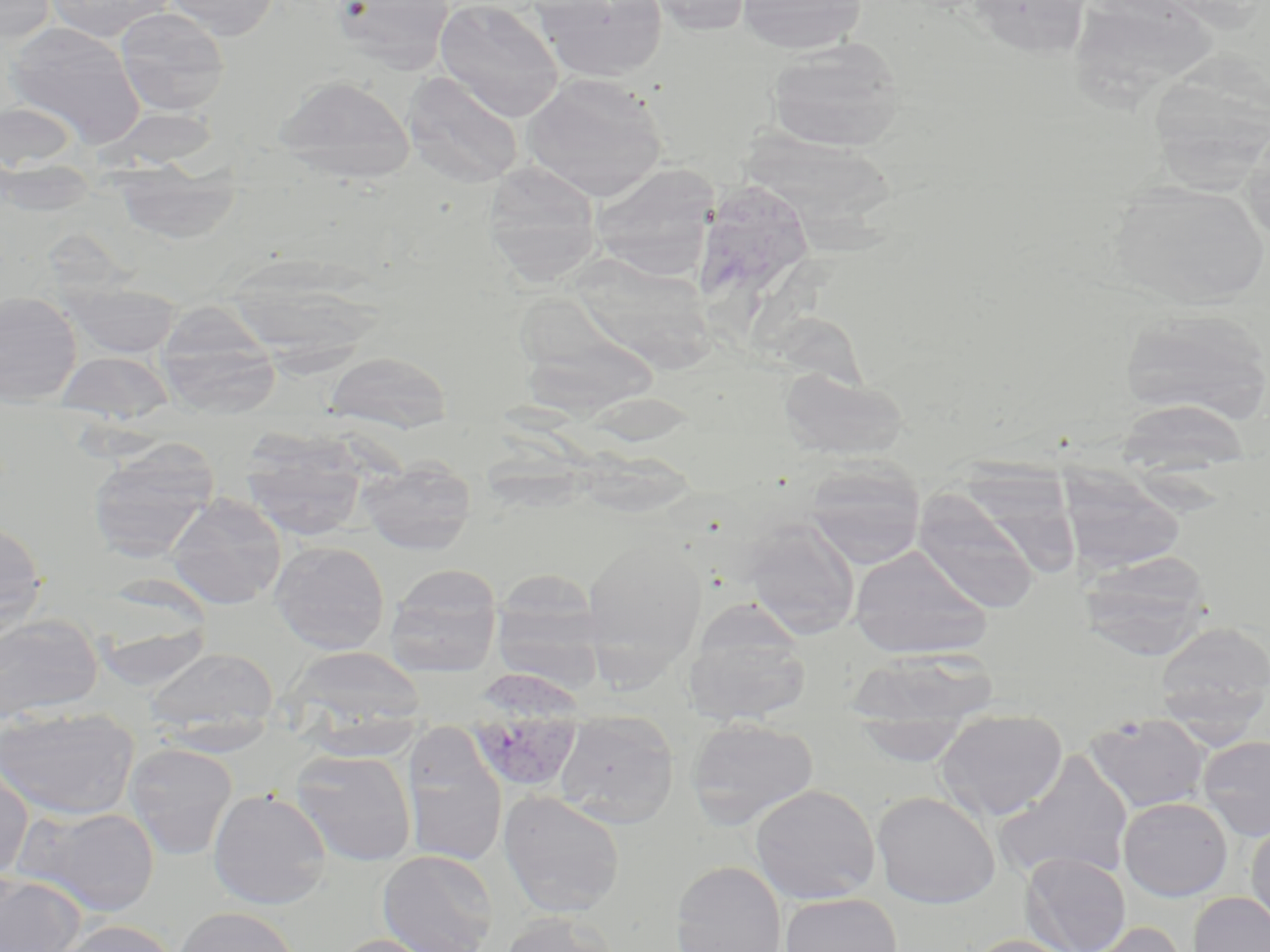

Summary:
  - Coordinate format: approximate bounding boxes as (x1,y1)-(x2,y2) corner pairs in pixels
  - Uninfected red blood cell locations: (0,0)-(56,44), (44,0)-(173,41), (162,0)-(280,40), (332,0)-(454,73), (434,0)-(564,121), (535,0)-(669,83), (643,0)-(754,36), (736,0)-(868,54), (966,0)-(1096,59), (1073,3)-(1223,117), (115,6)-(229,116), (5,21)-(146,147), (766,38)-(905,152), (1151,54)-(1270,206), (402,72)-(524,188), (521,73)-(668,201), (273,74)-(415,182), (0,101)-(79,173), (98,107)-(222,172), (1241,120)-(1270,244), (740,132)-(895,231), (112,158)-(240,245), (483,161)-(602,286), (590,163)-(722,279), (699,166)-(802,335), (1107,181)-(1268,309), (570,252)-(726,384), (229,256)-(389,379), (62,281)-(182,359), (0,291)-(83,406), (503,295)-(653,425), (155,304)-(281,417), (1119,308)-(1269,426), (56,351)-(175,425), (324,351)-(451,432), (779,367)-(908,461), (1115,399)-(1252,482), (239,428)-(372,541), (88,439)-(218,561), (358,456)-(477,555), (805,459)-(925,569), (960,466)-(1082,579), (1059,468)-(1186,576), (912,489)-(1040,614), (165,494)-(287,610), (0,520)-(48,639), (744,521)-(860,640), (582,535)-(707,678), (270,541)-(390,654), (849,545)-(990,659), (1079,550)-(1212,658), (385,565)-(502,675), (491,570)-(605,687), (0,613)-(103,723), (88,614)-(215,690), (684,615)-(810,726), (1155,621)-(1270,728), (282,646)-(425,739), (144,647)-(279,737), (848,649)-(997,731), (0,706)-(139,820), (935,708)-(1069,821), (555,712)-(679,827), (1085,712)-(1211,813), (854,714)-(972,767), (686,717)-(819,828), (402,729)-(507,867), (1198,735)-(1270,840), (124,743)-(237,860), (290,748)-(417,866), (995,752)-(1135,884), (0,761)-(33,882), (750,784)-(881,905), (208,788)-(332,909), (498,790)-(626,917), (871,790)-(1000,908), (1118,797)-(1233,901), (15,805)-(161,916), (1246,822)-(1270,934), (377,849)-(499,952), (1022,852)-(1130,952), (670,860)-(786,952), (0,872)-(85,952), (779,892)-(902,952), (1189,892)-(1270,952), (173,906)-(300,952), (497,911)-(619,952), (52,919)-(179,952), (1081,921)-(1187,952), (330,934)-(449,952), (961,934)-(1084,952)
  - Plasmodium vivax-infected red blood cell locations: (472,671)-(586,788)
  - Slide-level diagnosis: Plasmodium vivax
  - Preparation: thin blood film
  - Magnification: 1000x
  - Image size: 1270×952 pixels
  - Field of view: one of a larger specimen
  - Stain: May-Grünwald-Giemsa
  - Modality: optical microscopy